Describe the morphology of the red blood cells.
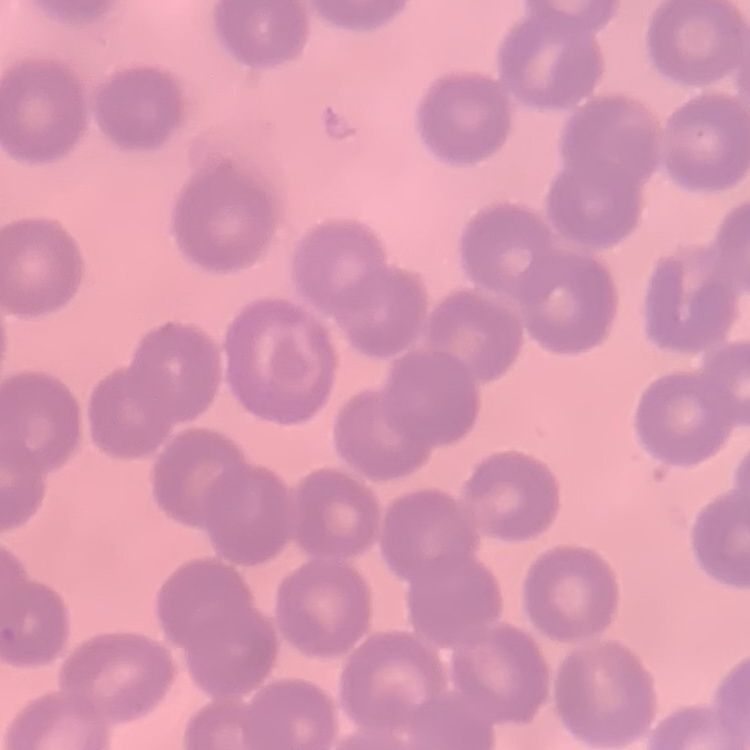
No rouleaux formation.

Field's or Giemsa stain. Thin peripheral smear. One tile cut from a larger photomicrograph.